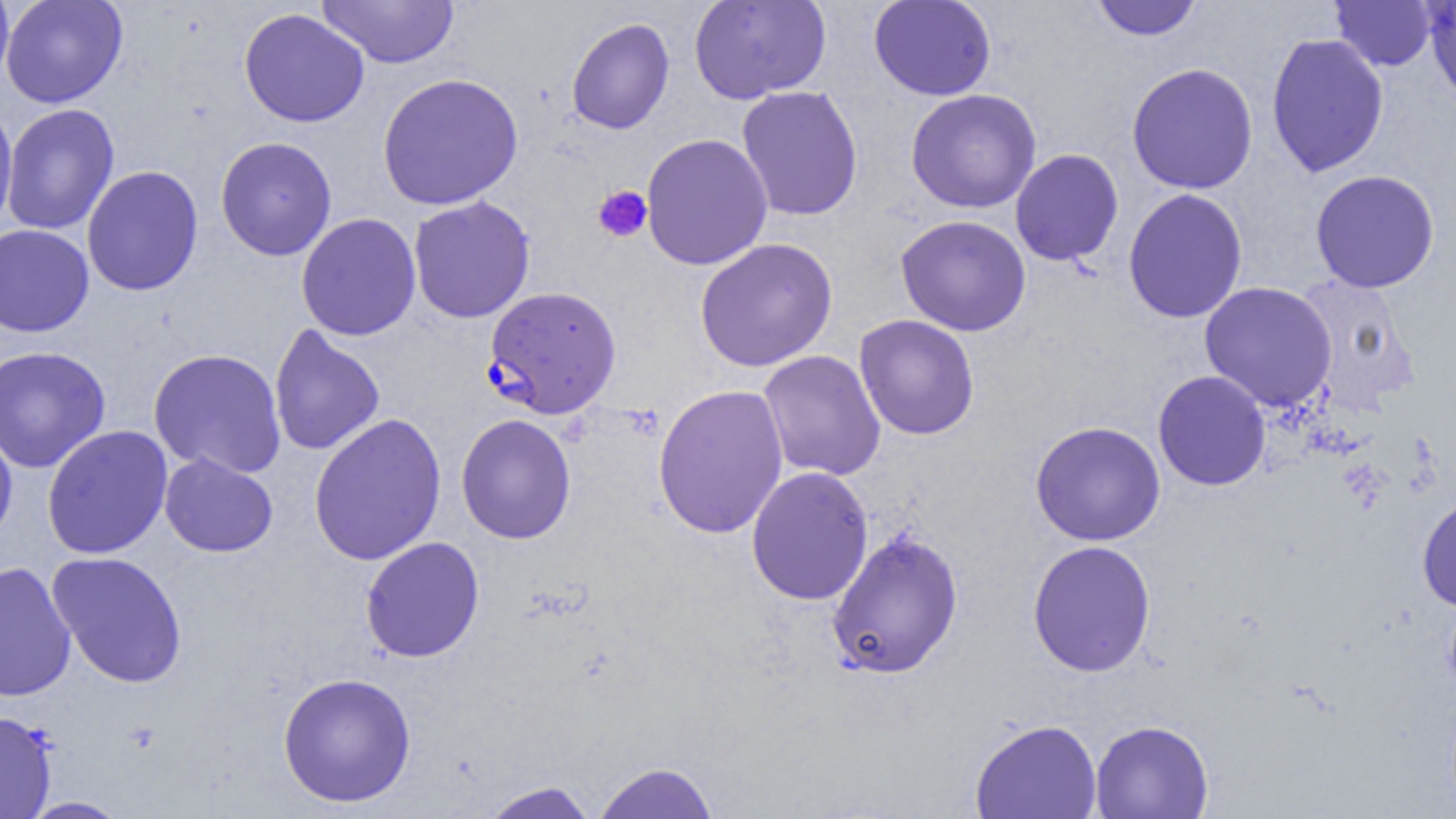 Approximate bounding boxes as [x1, y1, x2, y2] in pixels. Plasmodium falciparum-infected red blood cell locations: [484, 285, 622, 419]. Platelet locations: [593, 185, 653, 243]. Uninfected red blood cell locations: [0, 0, 128, 109], [0, 0, 14, 90], [316, 0, 459, 69], [689, 0, 831, 104], [868, 0, 997, 101], [1090, 0, 1203, 41], [1423, 0, 1456, 104], [1330, 1, 1438, 72], [239, 8, 370, 128], [566, 17, 675, 134], [1265, 33, 1390, 177], [1126, 62, 1259, 194], [377, 72, 523, 210], [736, 86, 864, 221], [905, 88, 1042, 213], [0, 101, 18, 237], [1, 103, 120, 236], [641, 133, 773, 270], [215, 136, 337, 261], [1009, 149, 1124, 266], [81, 165, 204, 296], [1310, 169, 1440, 293], [1122, 188, 1248, 324], [408, 195, 536, 323], [296, 213, 422, 341], [895, 214, 1032, 337], [0, 224, 94, 337], [694, 237, 838, 372], [1293, 273, 1420, 413], [1199, 281, 1338, 412], [854, 314, 980, 440], [269, 324, 384, 457], [0, 345, 111, 473], [147, 348, 286, 479], [758, 350, 886, 481], [1152, 370, 1271, 491], [652, 383, 790, 539], [308, 412, 447, 566], [455, 413, 576, 544], [1030, 420, 1166, 546], [0, 421, 18, 547], [42, 425, 173, 559], [159, 453, 278, 557], [746, 465, 874, 605], [1416, 494, 1456, 611], [825, 530, 964, 680], [360, 536, 485, 663], [1027, 540, 1157, 677], [47, 551, 188, 688], [0, 561, 77, 702], [277, 672, 416, 807], [0, 710, 57, 818], [969, 717, 1102, 819], [1090, 719, 1214, 818], [593, 761, 720, 818], [479, 781, 600, 819], [17, 796, 132, 818]. Slide-level diagnosis: Plasmodium falciparum. Light microscopy. Image is 1456×819 pixels. Thin blood film. Single field of view. Captured at 1000x magnification.